State which cell type is depicted.
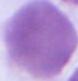
An erythrocyte.

magnification = 1000x
modality = micrograph